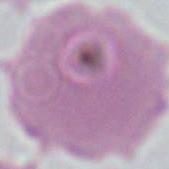
Summary:
  - Identification: red blood cell
  - Modality: photomicrograph
  - Magnification: 1000x